Report the malaria status of this cell.
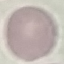

It is uninfected.

Photographed with a smartphone camera at the microscope eyepiece. Giemsa-stained preparation. Thin smear of blood. Automatically extracted cell patch, resized to 64 × 64 pixels.